Assess this cell for malaria.
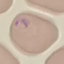
Parasitized.

image type = automatically extracted cell patch, resized to 64 × 64 pixels
capture = smartphone camera at the microscope eyepiece
preparation = thin blood smear
stain = Giemsa